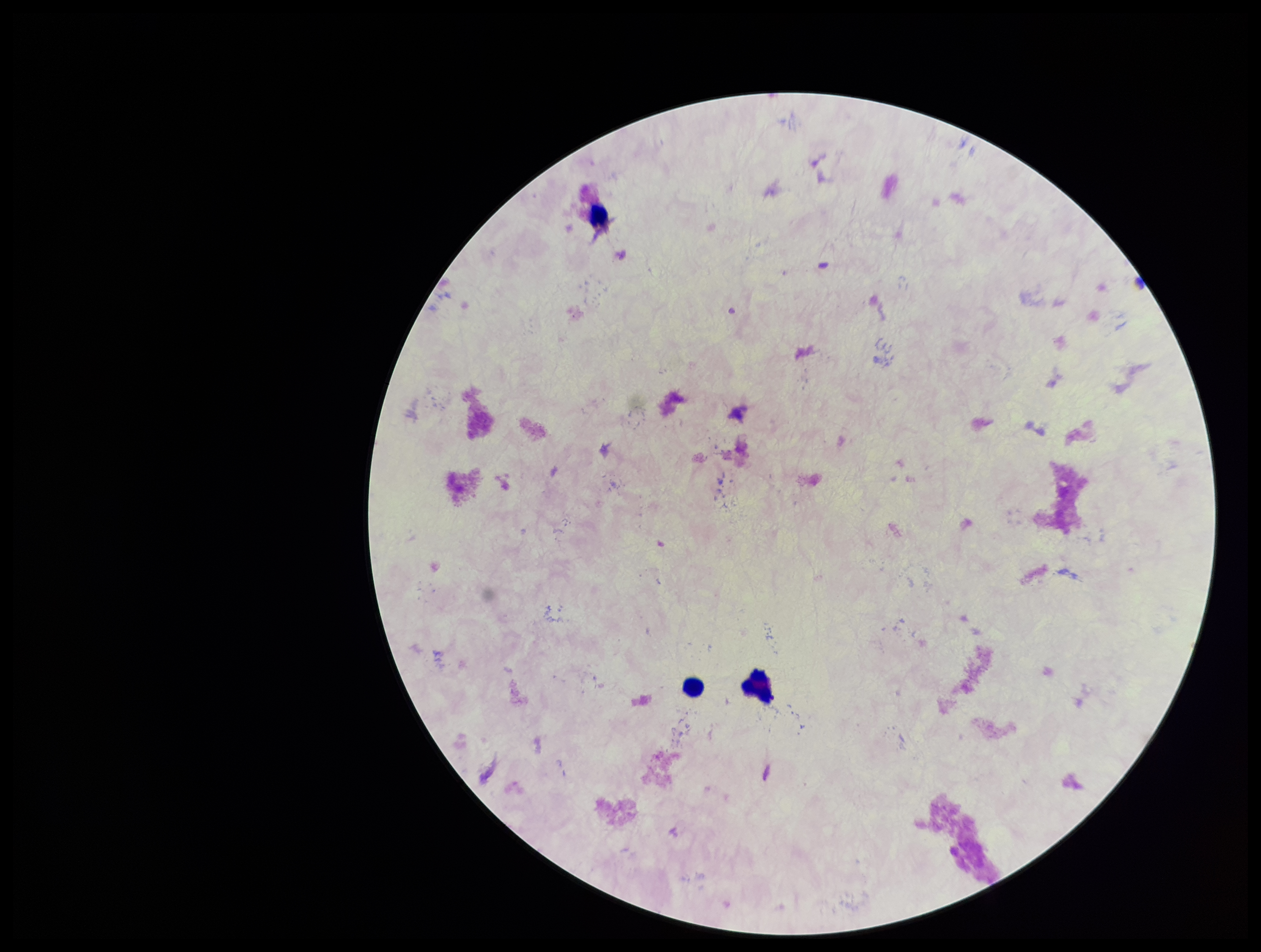
Summary:
  - Field of view: one from this slide
  - Patient malaria status: negative
  - Preparation: thick
  - Parasite count: 0
  - Plasmodium parasites: none identified
  - Leukocyte count: 3
  - Capture: smartphone photograph through the microscope eyepiece
  - Image size: 1261×952 pixels
  - Stain: Giemsa